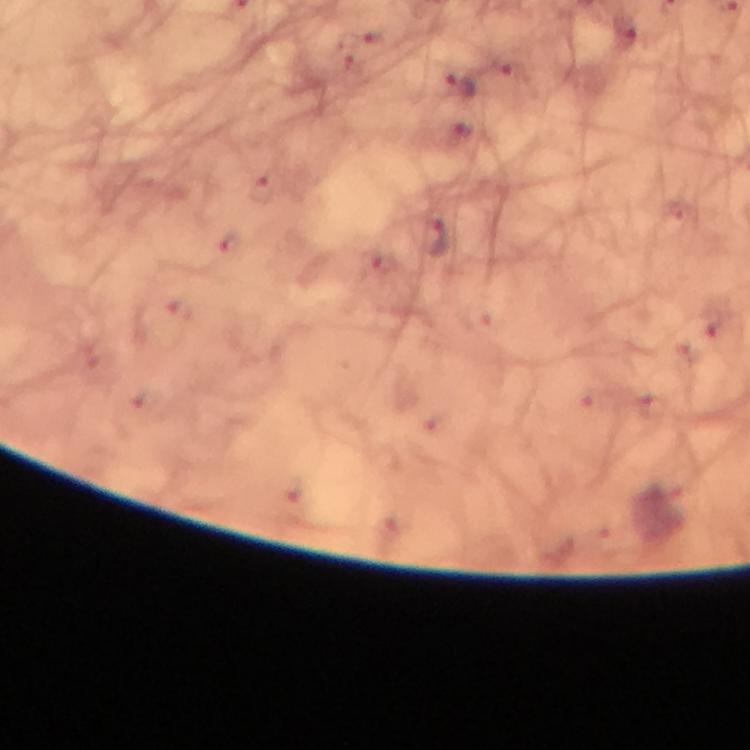 Approximate centers as [x, y] in pixels. Plasmodium parasite locations: [461, 83], [468, 131], [436, 239]. Giemsa-stained preparation. At 100x magnification. A crop from one field of view. From a malaria diagnostic workup. Image is 750×750 pixels. Immersion oil applied. Thick blood smear. Photographed with a smartphone mounted on the microscope.